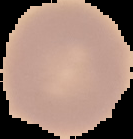
Summary:
  - Preparation: thin blood film
  - Image type: cell region segmented out of the field of view; surrounding area masked to black
  - Image size: 133×139 pixels
  - Result: negative for malaria parasites